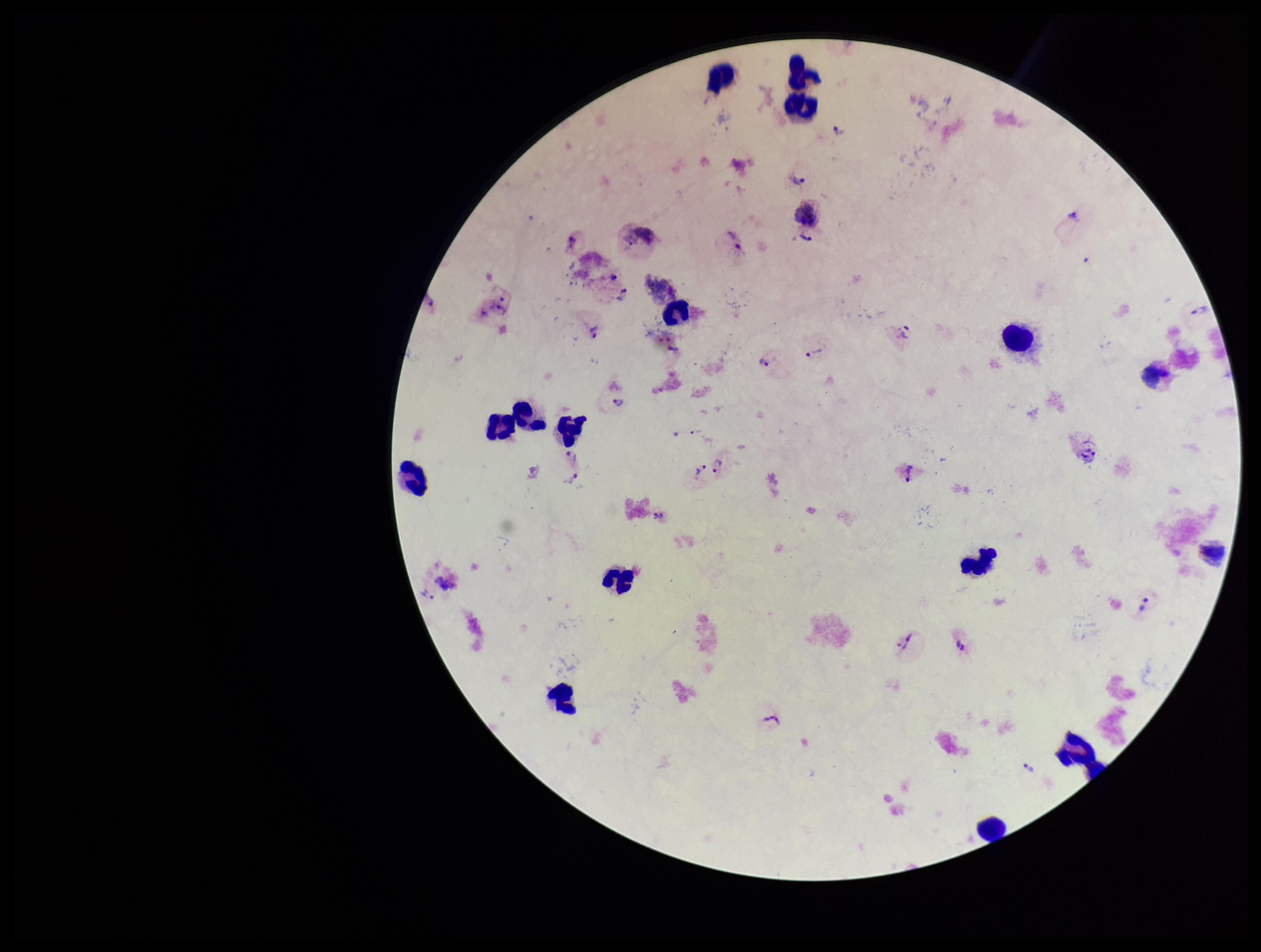

leukocyte count = 16
patient malaria status = infected
image size = 1261×952 pixels
field of view = single
stain = Giemsa
species reported for this patient = Plasmodium vivax
Plasmodium parasites = seen
parasite count = 29
capture = smartphone photograph through the microscope eyepiece
preparation = thick blood smear